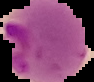
Image is 94×82 pixels. From a thin blood smear. Malaria status: parasitized. Segmented cell region on a black background.